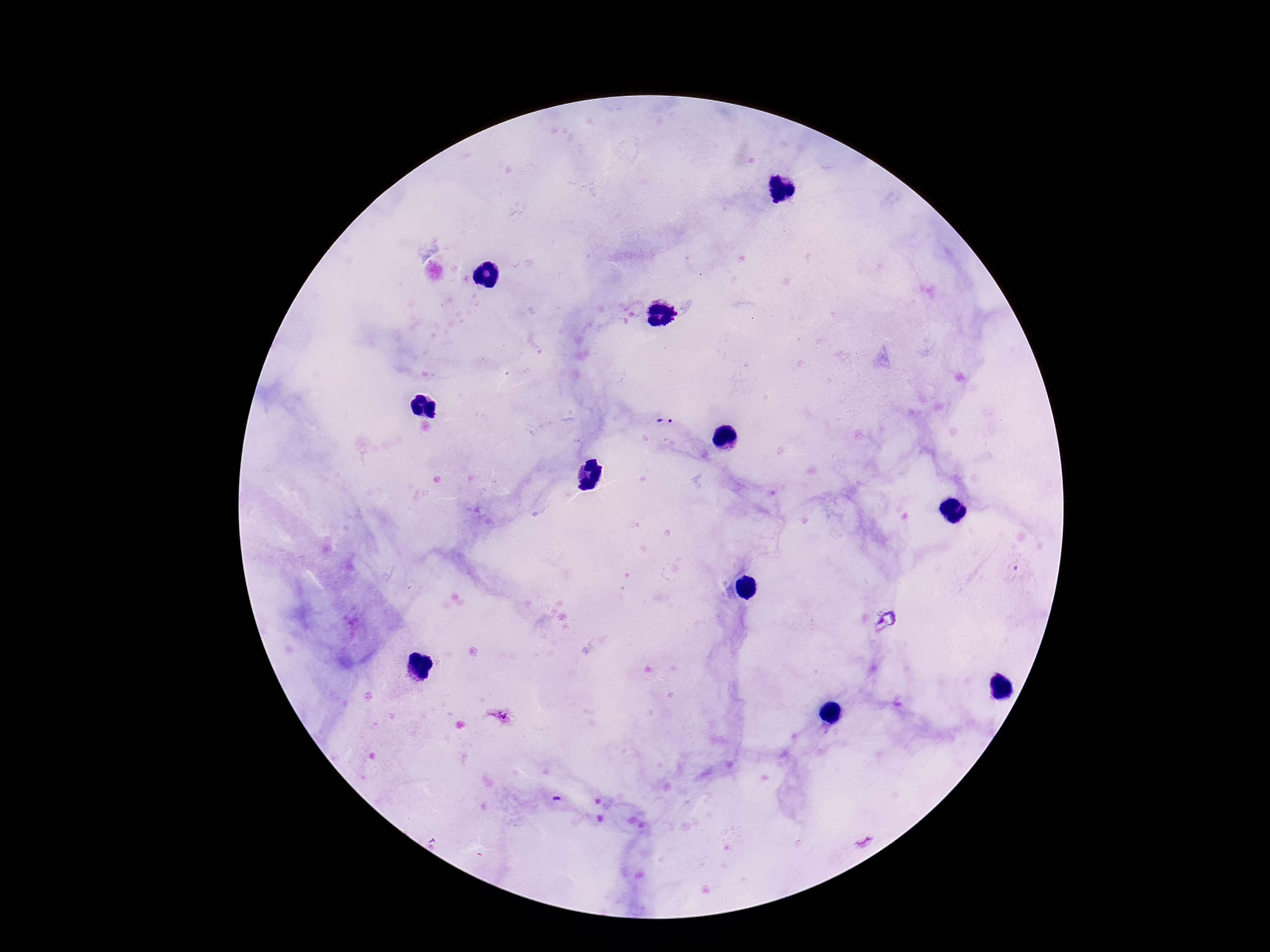 Approximate centers as {x, y} in pixels. Plasmodium parasite locations: {667, 422}. Photographed through the microscope eyepiece with a smartphone camera. Thick blood film. Patient malaria status: infected. One field from this slide. 100x magnification. Giemsa-stained preparation. Image is 1270×952 pixels.